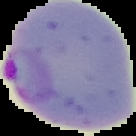 Malaria status: parasitized. From a thin blood film. Image is 136×136 pixels. Segmented cell region on a black background.